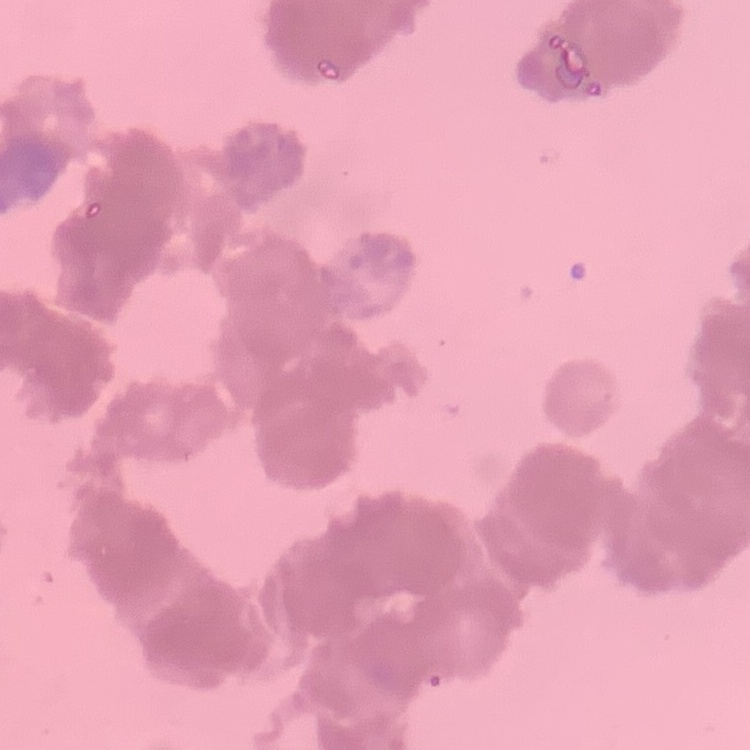
erythrocyte morphology = rouleaux formation
image type = one tile cut from a larger photomicrograph
stain = Field's or Giemsa
preparation = thin peripheral smear